Assess this cell for malaria.
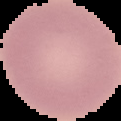
It is uninfected.

From a thin blood film. Image is 121×121 pixels. The area outside the segmented cell region is set to black.